Describe the morphology of the red blood cells.
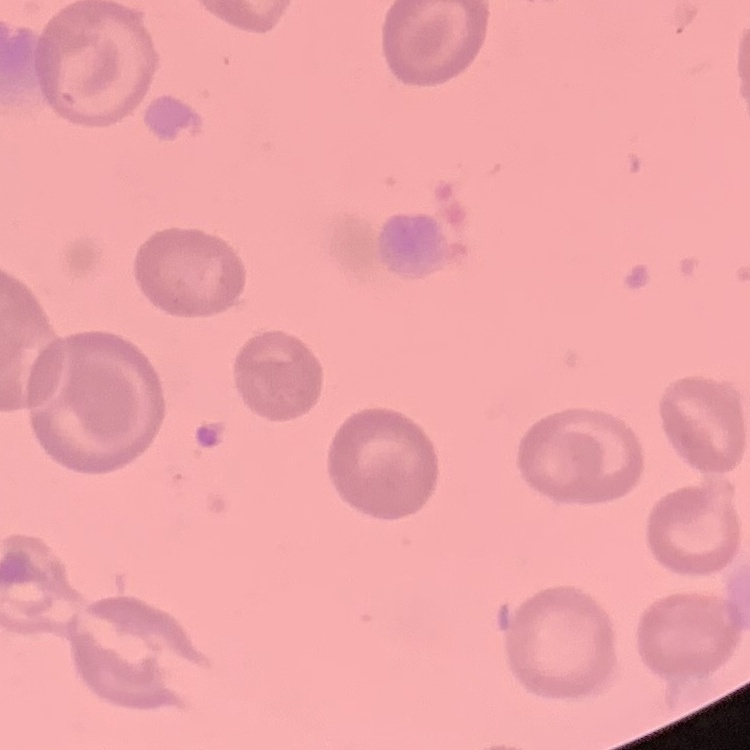

They show no rouleaux formation.

{
  "preparation": "thin blood smear",
  "image_type": "square crop of a larger photomicrograph",
  "stain": "Field's or Giemsa"
}